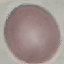
malaria status = uninfected
preparation = thin blood smear
image type = cell patch, automatically extracted from a larger field of view and resized to 64 × 64 pixels
stain = Giemsa
capture = smartphone through the microscope eyepiece